Report the malaria status of this cell.
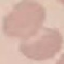

It is uninfected.

Cell patch, automatically extracted from a larger field of view and resized to 64 × 64 pixels. Acquired by smartphone through the microscope eyepiece. Giemsa stain. Thin smear of blood.